Name the parasite shown.
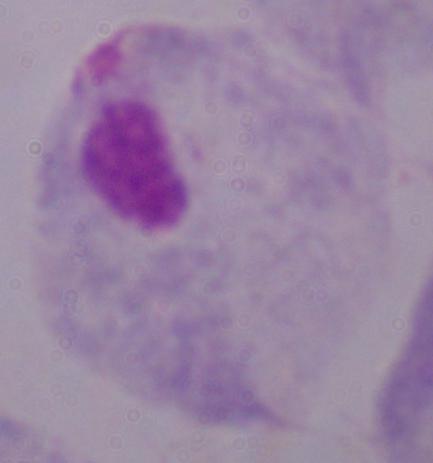

A trichomonad.

{
  "magnification": "1000x",
  "modality": "photomicrograph"
}